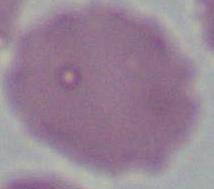
Photomicrograph. 1000x magnification. A red blood cell is seen.